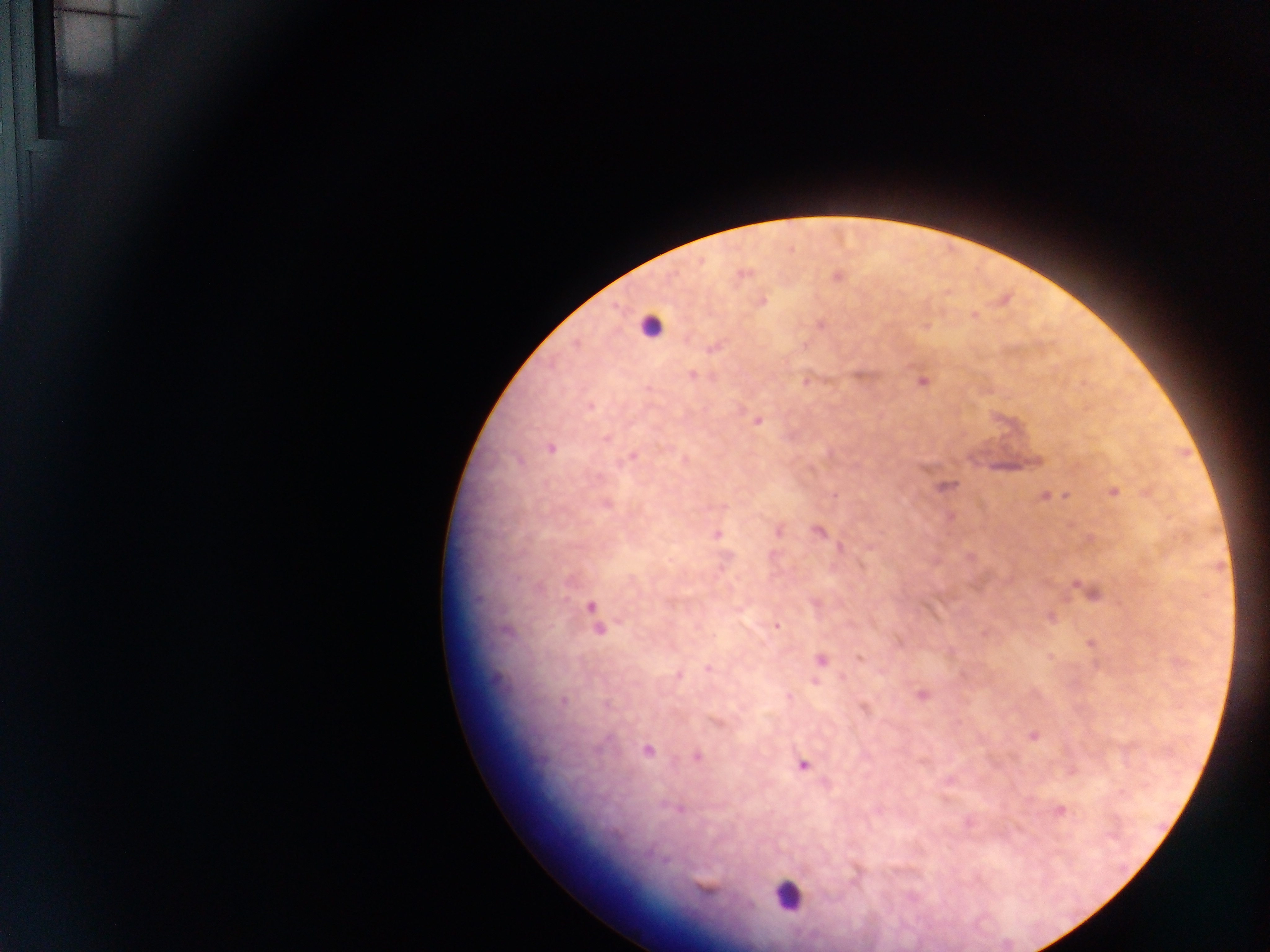
Approximate centers as {x, y} in pixels. Leukocyte locations: {649, 326}, {787, 897}. Plasmodium parasite locations: {837, 277}, {762, 302}, {973, 316}, {821, 324}, {713, 348}, {692, 375}, {923, 382}, {590, 405}, {758, 420}, {605, 438}, {551, 449}, {632, 457}, {948, 485}, {1114, 492}, {1046, 496}, {819, 532}, {717, 534}, {1090, 592}, {592, 607}, {777, 626}, {597, 630}, {1091, 643}, {860, 659}, {821, 660}, {708, 668}, {678, 675}, {815, 682}, {923, 695}, {562, 701}, {865, 707}, {1033, 736}, {647, 750}, {697, 756}, {804, 765}, {1060, 811}. Mobile-phone photograph taken through the microscope. Collected in Ghana. Thick blood film. One field of view. Image is 1270×952 pixels.